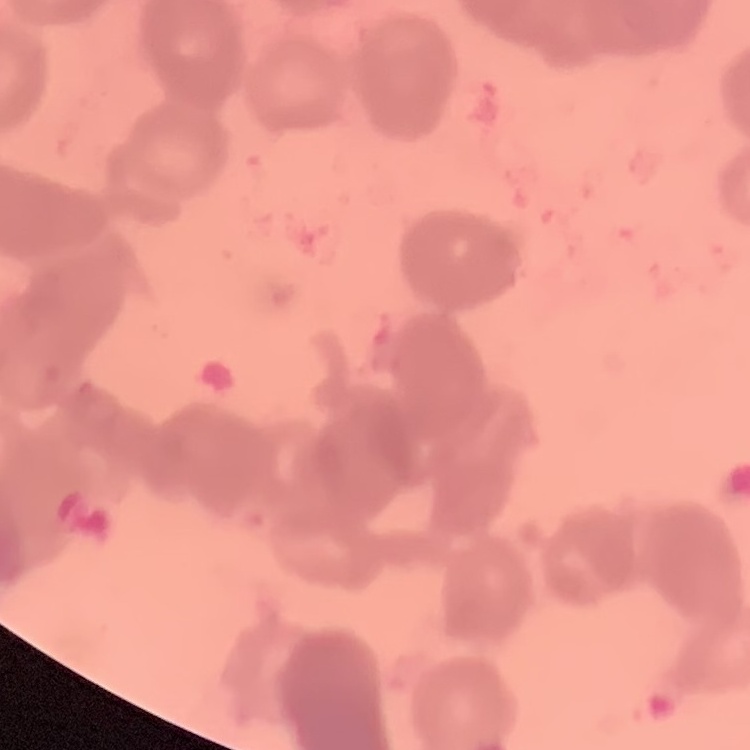
The erythrocytes show rouleaux formation. Stained with either Field's or Giemsa. Thin blood smear. Square crop of a larger photomicrograph.